Comment on the morphology of the red blood cells.
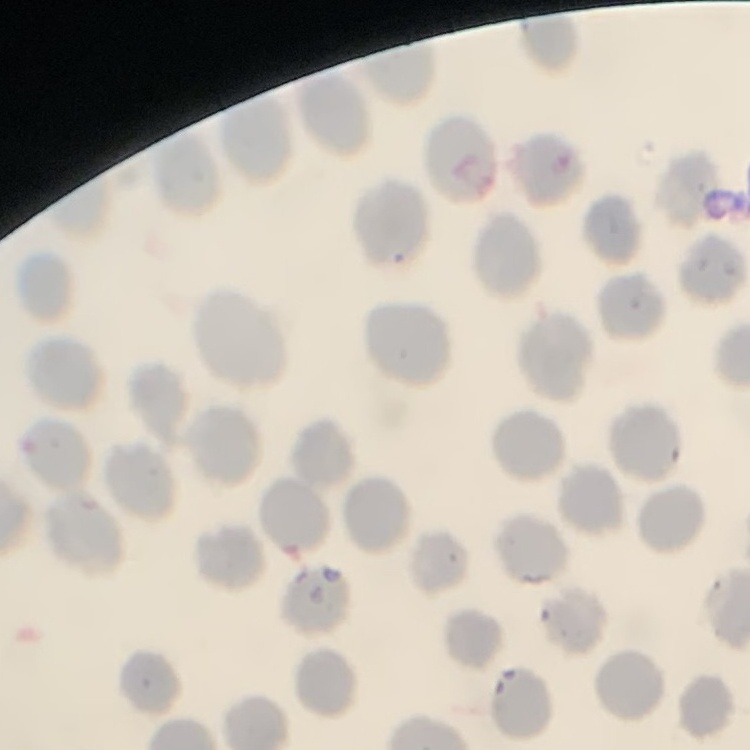

No rouleaux formation.

preparation = thin blood film
image type = one tile cut from a larger photomicrograph
stain = Field's or Giemsa